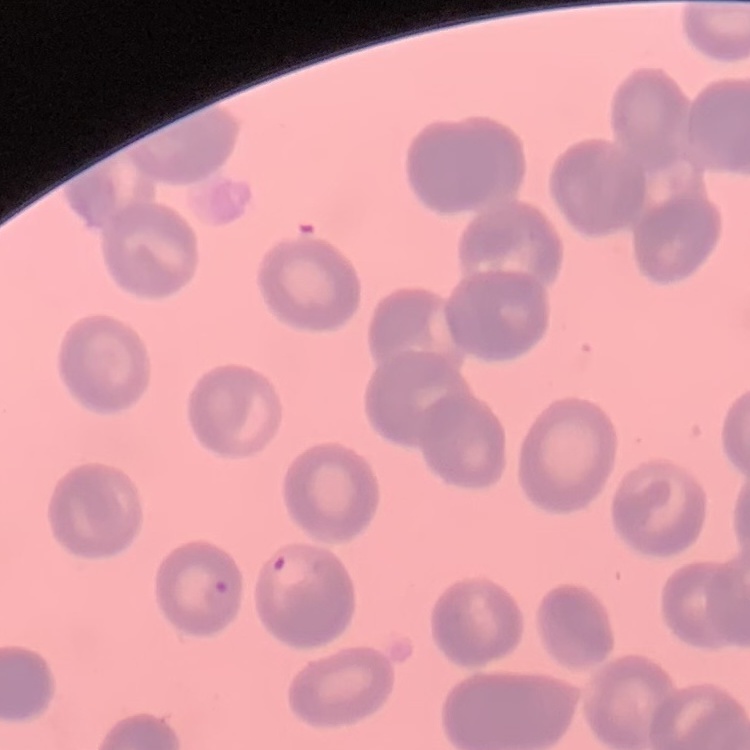

red blood cell morphology = no rouleaux formation
stain = Field's or Giemsa
image type = one tile cut from a larger photomicrograph
preparation = thin blood smear